Name the cell type shown.
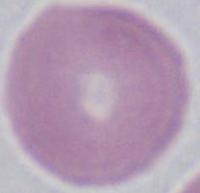

This is an erythrocyte.

Micrograph. Captured at 1000x magnification.